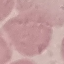

Result: negative for malaria parasites. Thin blood film. Giemsa-stained preparation. Automatically extracted cell patch, resized to 64 × 64 pixels. Acquired by smartphone through the microscope eyepiece.